State which parasite is depicted.
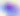
This is Toxoplasma gondii.

magnification = 400x
modality = micrograph